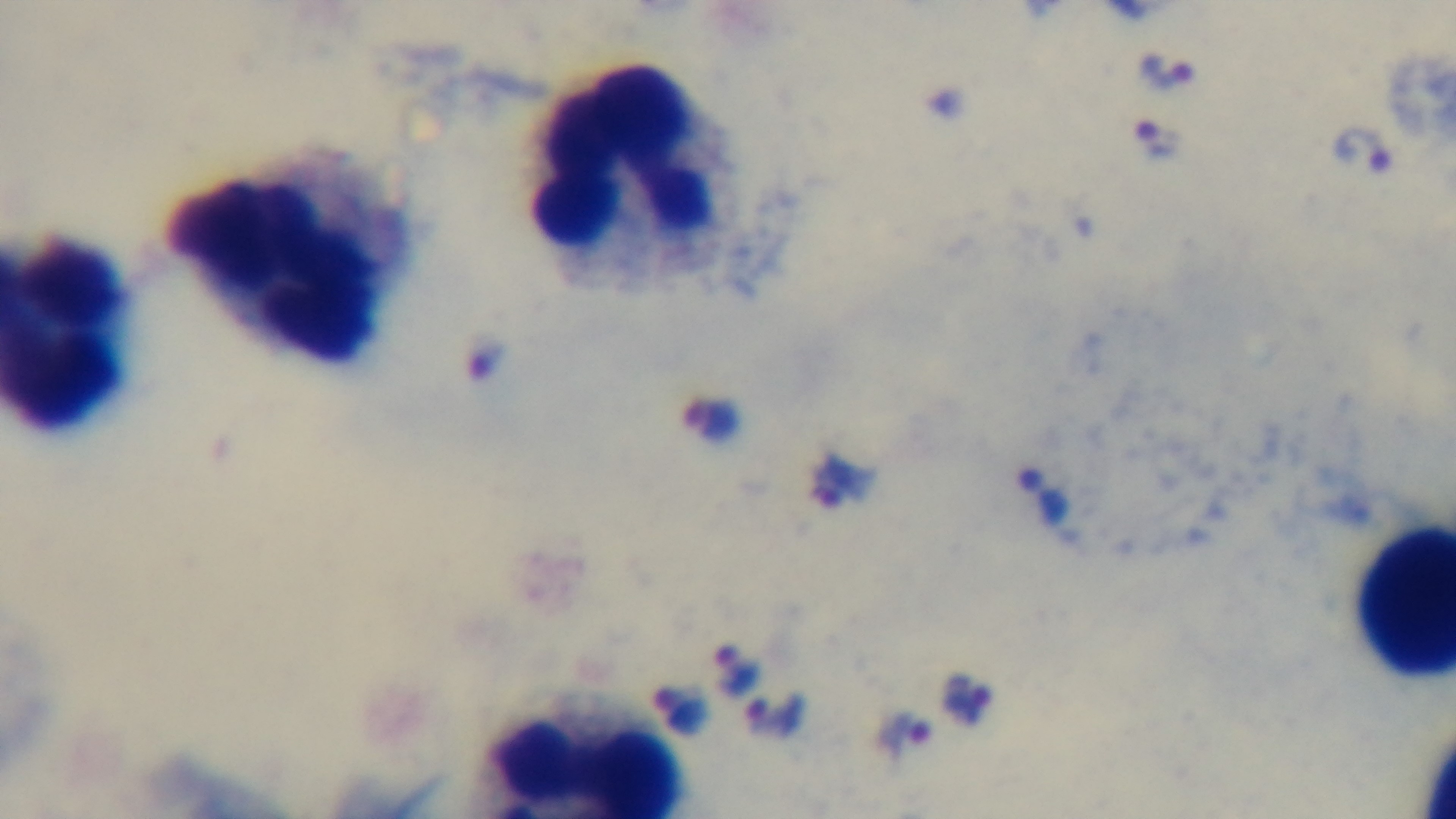
Summary:
  - Capture: mounted 4K digital camera
  - Field of view: single
  - Objective: 100x oil immersion
  - Modality: light microscopy
  - Stain: Giemsa
  - Preparation: thick smear
  - Malaria status: infected